State which parasite is depicted.
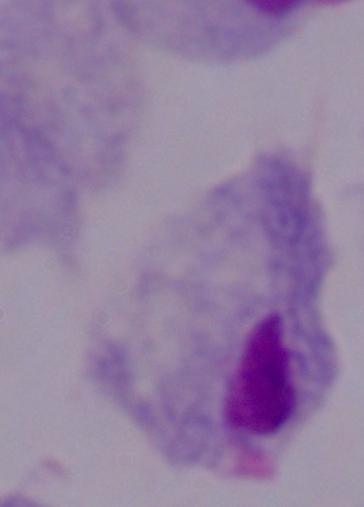

This is a trichomonad.

modality: photomicrograph
magnification: 1000x